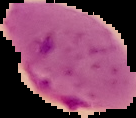
preparation = thin blood film
image size = 136×118 pixels
image type = segmented cell region on a black background
malaria status = parasitized